Name the blood parasite species.
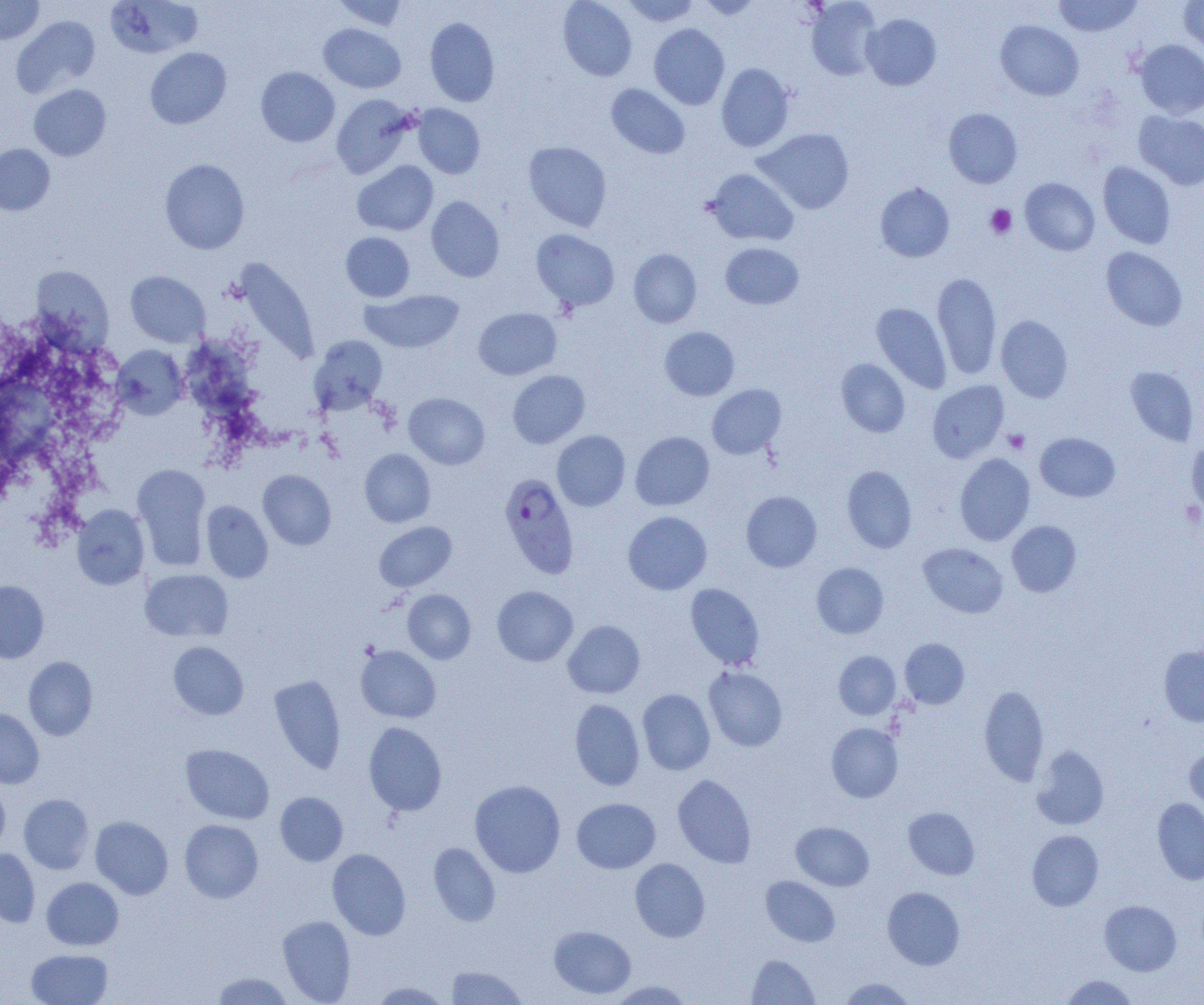
Plasmodium falciparum.

platelet_locations: 'approximate bounding boxes as named x1/y1/x2/y2 corners in pixels: (x1=986, y1=205, x2=1017, y2=239), (x1=1003, y1=429, x2=1030, y2=453)'
uninfected_red_blood_cell_locations: 'approximate bounding boxes as named x1/y1/x2/y2 corners in pixels: (x1=0, y1=0, x2=45, y2=45), (x1=331, y1=0, x2=409, y2=31), (x1=558, y1=0, x2=637, y2=81), (x1=621, y1=0, x2=700, y2=26), (x1=695, y1=0, x2=763, y2=21), (x1=806, y1=0, x2=882, y2=80), (x1=1052, y1=0, x2=1143, y2=37), (x1=1179, y1=0, x2=1204, y2=55), (x1=106, y1=1, x2=203, y2=58), (x1=861, y1=13, x2=941, y2=90), (x1=12, y1=15, x2=100, y2=97), (x1=425, y1=17, x2=500, y2=106), (x1=996, y1=20, x2=1083, y2=101), (x1=649, y1=23, x2=730, y2=109), (x1=318, y1=24, x2=406, y2=93), (x1=1135, y1=39, x2=1204, y2=118), (x1=145, y1=47, x2=231, y2=129), (x1=716, y1=63, x2=794, y2=152), (x1=256, y1=67, x2=339, y2=147), (x1=606, y1=83, x2=690, y2=159), (x1=29, y1=84, x2=111, y2=161), (x1=332, y1=94, x2=416, y2=179), (x1=413, y1=104, x2=485, y2=179), (x1=943, y1=108, x2=1023, y2=188), (x1=1134, y1=111, x2=1204, y2=189), (x1=755, y1=128, x2=854, y2=214), (x1=523, y1=141, x2=612, y2=231), (x1=0, y1=144, x2=55, y2=216), (x1=160, y1=159, x2=249, y2=254), (x1=353, y1=161, x2=438, y2=236), (x1=1098, y1=162, x2=1176, y2=249), (x1=705, y1=168, x2=799, y2=246), (x1=1020, y1=178, x2=1100, y2=255), (x1=875, y1=183, x2=954, y2=262), (x1=426, y1=196, x2=504, y2=282), (x1=531, y1=229, x2=619, y2=311), (x1=341, y1=232, x2=414, y2=302), (x1=720, y1=242, x2=804, y2=310), (x1=1101, y1=247, x2=1187, y2=331), (x1=628, y1=249, x2=702, y2=328), (x1=233, y1=257, x2=319, y2=366), (x1=31, y1=265, x2=113, y2=350), (x1=125, y1=271, x2=210, y2=347), (x1=932, y1=272, x2=1002, y2=379), (x1=361, y1=289, x2=464, y2=353), (x1=871, y1=302, x2=951, y2=393), (x1=473, y1=307, x2=561, y2=380), (x1=996, y1=315, x2=1073, y2=402), (x1=660, y1=326, x2=739, y2=400), (x1=309, y1=335, x2=388, y2=415), (x1=113, y1=345, x2=189, y2=419), (x1=836, y1=359, x2=910, y2=437), (x1=1125, y1=366, x2=1199, y2=446), (x1=507, y1=370, x2=590, y2=448), (x1=927, y1=380, x2=1009, y2=462), (x1=707, y1=384, x2=786, y2=459), (x1=404, y1=392, x2=489, y2=469), (x1=552, y1=430, x2=630, y2=511), (x1=630, y1=431, x2=714, y2=510), (x1=1035, y1=432, x2=1120, y2=501), (x1=1187, y1=441, x2=1204, y2=514), (x1=359, y1=449, x2=435, y2=527), (x1=954, y1=453, x2=1035, y2=545), (x1=132, y1=464, x2=211, y2=569), (x1=842, y1=466, x2=917, y2=553), (x1=257, y1=470, x2=336, y2=550), (x1=741, y1=491, x2=822, y2=572), (x1=201, y1=501, x2=273, y2=582), (x1=72, y1=504, x2=149, y2=590), (x1=623, y1=511, x2=712, y2=595), (x1=1006, y1=520, x2=1081, y2=597), (x1=374, y1=521, x2=456, y2=592), (x1=918, y1=543, x2=1008, y2=618), (x1=812, y1=562, x2=889, y2=638), (x1=139, y1=569, x2=233, y2=642), (x1=0, y1=580, x2=49, y2=662), (x1=685, y1=583, x2=764, y2=670), (x1=492, y1=586, x2=578, y2=666), (x1=402, y1=589, x2=476, y2=663), (x1=563, y1=620, x2=645, y2=698), (x1=900, y1=638, x2=969, y2=708), (x1=168, y1=641, x2=248, y2=720), (x1=356, y1=645, x2=440, y2=722), (x1=1159, y1=646, x2=1204, y2=726), (x1=834, y1=651, x2=900, y2=719), (x1=23, y1=656, x2=98, y2=740), (x1=704, y1=666, x2=787, y2=751), (x1=268, y1=675, x2=346, y2=774), (x1=979, y1=684, x2=1048, y2=786), (x1=637, y1=689, x2=715, y2=775), (x1=570, y1=698, x2=644, y2=791), (x1=0, y1=709, x2=44, y2=789), (x1=363, y1=721, x2=447, y2=816), (x1=827, y1=723, x2=903, y2=803), (x1=180, y1=744, x2=274, y2=823), (x1=1031, y1=746, x2=1109, y2=830), (x1=1185, y1=747, x2=1204, y2=816), (x1=672, y1=774, x2=756, y2=868), (x1=470, y1=780, x2=565, y2=877), (x1=0, y1=783, x2=10, y2=853), (x1=275, y1=792, x2=348, y2=866), (x1=19, y1=793, x2=94, y2=874), (x1=572, y1=798, x2=660, y2=873), (x1=1153, y1=798, x2=1204, y2=884), (x1=903, y1=807, x2=980, y2=880), (x1=90, y1=816, x2=173, y2=899), (x1=179, y1=819, x2=263, y2=902), (x1=791, y1=821, x2=874, y2=890), (x1=1027, y1=829, x2=1103, y2=911), (x1=428, y1=843, x2=500, y2=926), (x1=0, y1=848, x2=40, y2=927), (x1=327, y1=848, x2=410, y2=940), (x1=630, y1=858, x2=710, y2=942), (x1=761, y1=876, x2=840, y2=946), (x1=42, y1=877, x2=123, y2=950), (x1=882, y1=886, x2=965, y2=970), (x1=1100, y1=900, x2=1181, y2=975), (x1=277, y1=916, x2=356, y2=1004), (x1=549, y1=926, x2=636, y2=999), (x1=27, y1=949, x2=112, y2=1005), (x1=747, y1=954, x2=819, y2=1004), (x1=446, y1=965, x2=527, y2=1004), (x1=210, y1=972, x2=295, y2=1004), (x1=1060, y1=975, x2=1137, y2=1004), (x1=839, y1=977, x2=916, y2=1004), (x1=606, y1=980, x2=694, y2=1004), (x1=367, y1=981, x2=452, y2=1004)'
magnification: 1000x
field_of_view: single
image_size: 1204×1005 pixels
modality: light microscopy
preparation: thin blood film
plasmodium_falciparum_infected_red_blood_cell_locations: 'approximate bounding boxes as named x1/y1/x2/y2 corners in pixels: (x1=499, y1=472, x2=579, y2=579)'